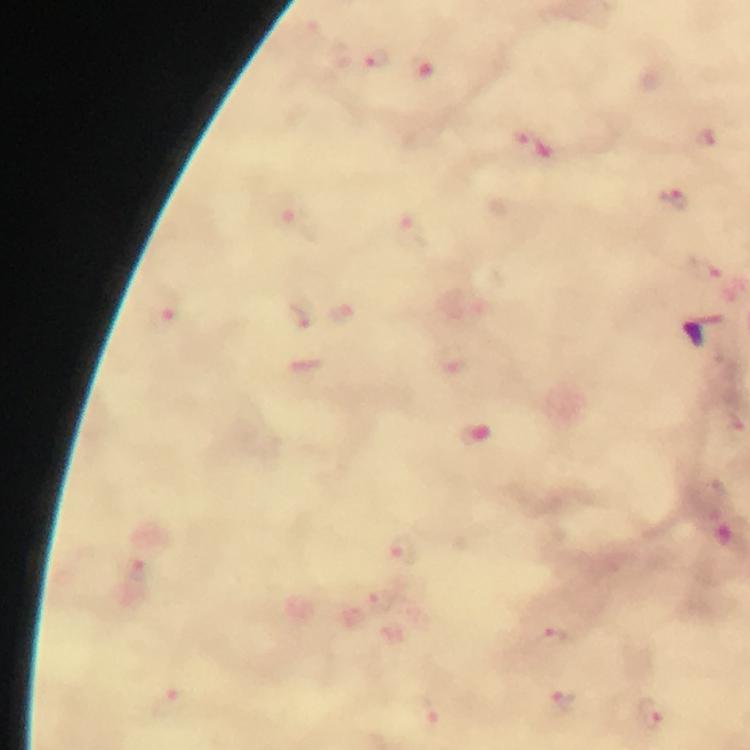

capture = smartphone mounted on the microscope
stain = Giemsa
magnification = 100x
cropped from = one field of view
immersion oil = applied
image size = 750×750 pixels
context = from a malaria diagnostic workup
malaria parasite locations = approximate centers as {x, y} in pixels: {375, 60}, {422, 71}, {522, 134}, {706, 137}, {675, 199}, {294, 221}, {410, 228}, {165, 314}, {297, 317}, {346, 318}, {402, 549}, {132, 566}, {379, 601}, {551, 639}, {171, 703}, {564, 703}, {650, 714}, {426, 716}
preparation = thick smear